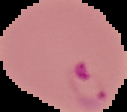 Image is 127×112 pixels. From a thin blood smear. Malaria status: parasitized. Segmented cell region on a black background.